Classify this cell by malaria status.
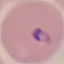

It is parasitized.

Acquired by smartphone through the microscope eyepiece. Giemsa-stained preparation. Thin blood film. Cell patch, automatically extracted from a larger field of view and resized to 64 × 64 pixels.